Describe the morphology of the erythrocytes.
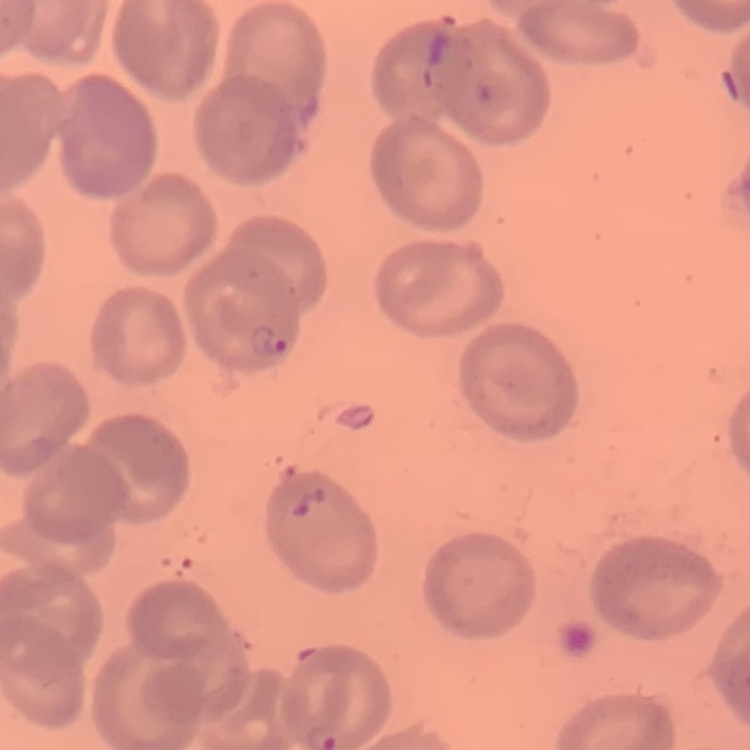
No rouleaux formation.

One tile cut from a larger photomicrograph. Thin blood film. Field's or Giemsa stain.